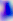

Micrograph. Toxoplasma gondii is seen. Captured at 400x magnification.